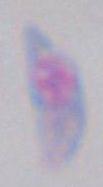
identification = Toxoplasma gondii
modality = photomicrograph
magnification = 1000x